Comment on the morphology of the erythrocytes.
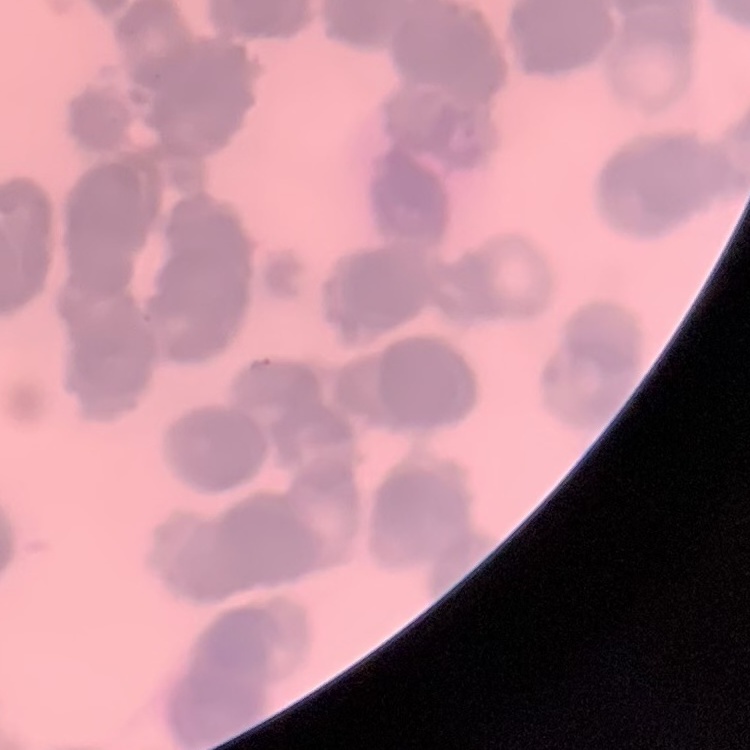

They show rouleaux formation.

{
  "stain": "Field's or Giemsa",
  "preparation": "thin peripheral smear",
  "image_type": "one tile cut from a larger photomicrograph"
}